Assess this cell for malaria.
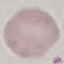
It is uninfected.

Cell patch, automatically extracted from a larger field of view and resized to 64 × 64 pixels. Photographed with a smartphone camera at the microscope eyepiece. Giemsa-stained preparation. Thin blood smear.